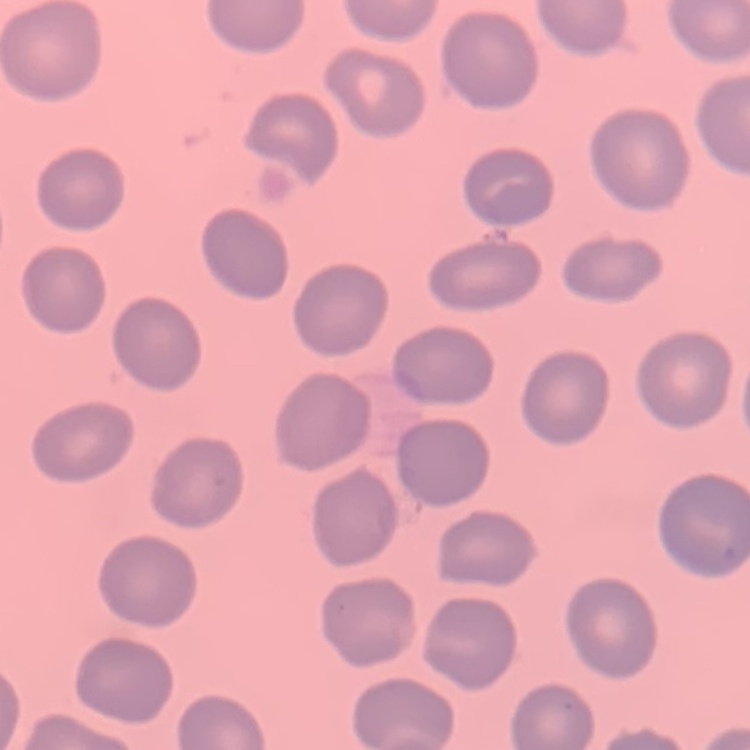
erythrocyte_morphology: no rouleaux formation
image_type: square crop of a larger photomicrograph
preparation: thin blood smear
stain: Field's or Giemsa